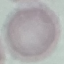

Result: negative for malaria parasites. Thin blood smear. Giemsa-stained preparation. Acquired by smartphone through the microscope eyepiece. Automatically extracted cell patch, resized to 64 × 64 pixels.